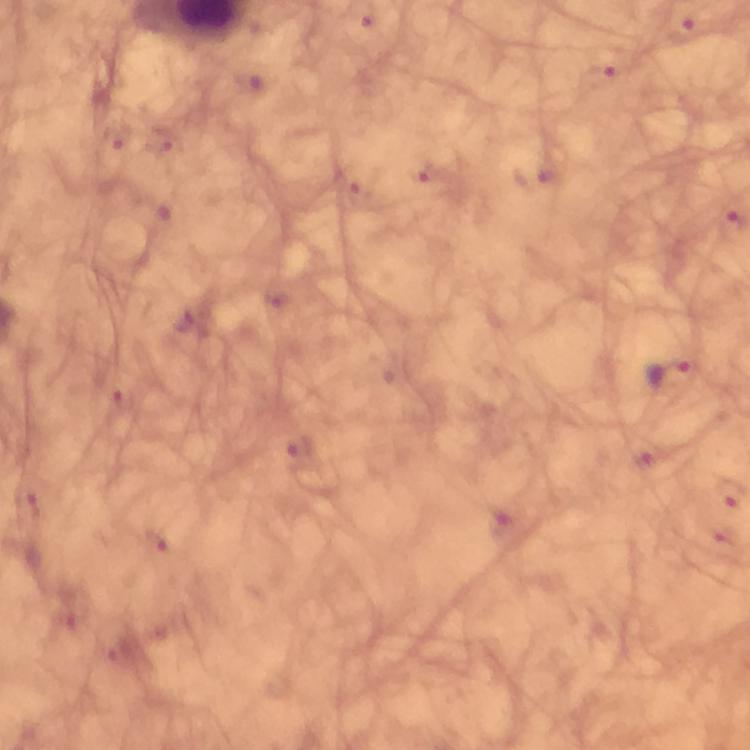

Approximate centers as {x, y} in pixels. Plasmodium parasite locations: {667, 372}. Image is 750×750 pixels. Thick blood smear. 100x magnification. Giemsa stain. Photographed with a smartphone mounted on the microscope. From a diagnostic examination for malaria. Cropped region of a single field of view. Immersion oil was used.